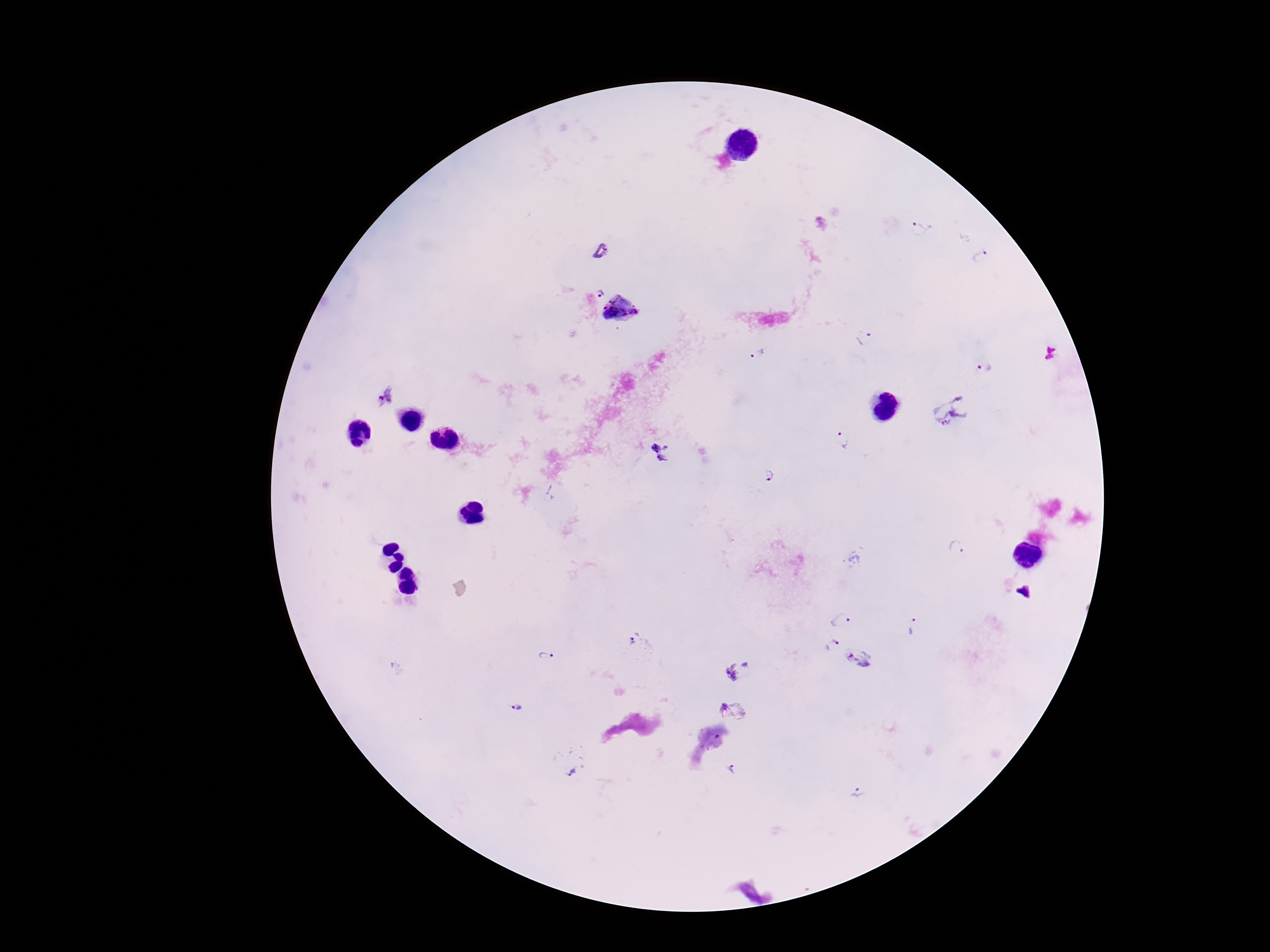

Approximate object centers, in pixels from the top-left corner.
Summary:
  - Plasmodium parasite locations: (x=920, y=229), (x=602, y=251), (x=981, y=256), (x=600, y=293), (x=622, y=309), (x=865, y=338), (x=759, y=355), (x=987, y=368), (x=385, y=393), (x=951, y=411), (x=841, y=439), (x=662, y=451), (x=770, y=472), (x=957, y=548), (x=842, y=620), (x=912, y=626), (x=637, y=643), (x=832, y=645), (x=547, y=656), (x=857, y=658), (x=738, y=671), (x=516, y=707), (x=731, y=711), (x=569, y=764), (x=729, y=769), (x=859, y=794)
  - Preparation: thick blood film
  - Patient malaria status: positive
  - Magnification: 100x
  - Image size: 1270×952 pixels
  - Capture: smartphone camera through the microscope eyepiece
  - Stain: Giemsa
  - Field of view: single